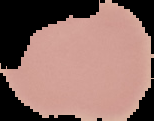
image size = 154×121 pixels
malaria status = uninfected
image type = cell region segmented out of the field of view; surrounding area masked to black
preparation = thin blood smear